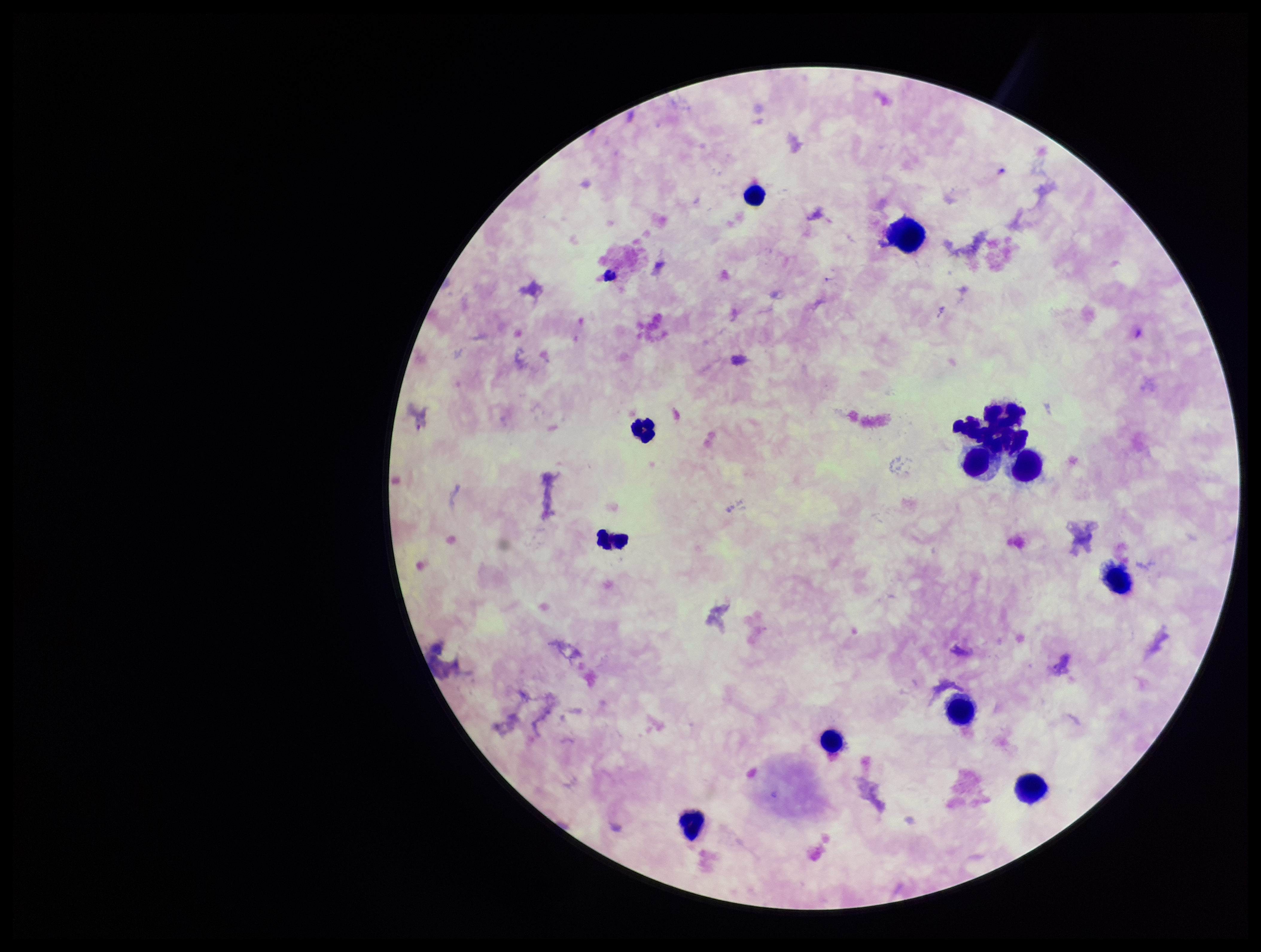 Patient malaria status: infected. One field from this slide. Leukocyte count: 13. Species reported for this patient: Plasmodium falciparum. Preparation: thick. Photographed through the microscope eyepiece with a smartphone camera. Stained with Giemsa. Parasite count: 0. Image is 1261×952 pixels. Plasmodium parasites: none detected.